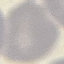

Malaria status: uninfected. Cell patch, automatically extracted from a larger field of view and resized to 64 × 64 pixels. Photographed with a smartphone camera at the microscope eyepiece. Giemsa stain. Thin blood smear.